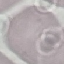
Result: negative for malaria parasites. Automatically extracted cell patch, resized to 64 × 64 pixels. Thin blood smear. Giemsa stain. Acquired by smartphone through the microscope eyepiece.